Assess this cell for malaria.
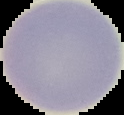

It is uninfected.

Segmented cell region on a black background. Image is 124×115 pixels. From a thin blood smear.